Assess this cell for malaria.
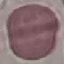

Uninfected.

preparation = thin smear
image type = automatically extracted cell patch, resized to 64 × 64 pixels
capture = smartphone through the microscope eyepiece
stain = Giemsa